State which parasite is depicted.
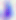

Toxoplasma gondii.

magnification: 400x
modality: photomicrograph